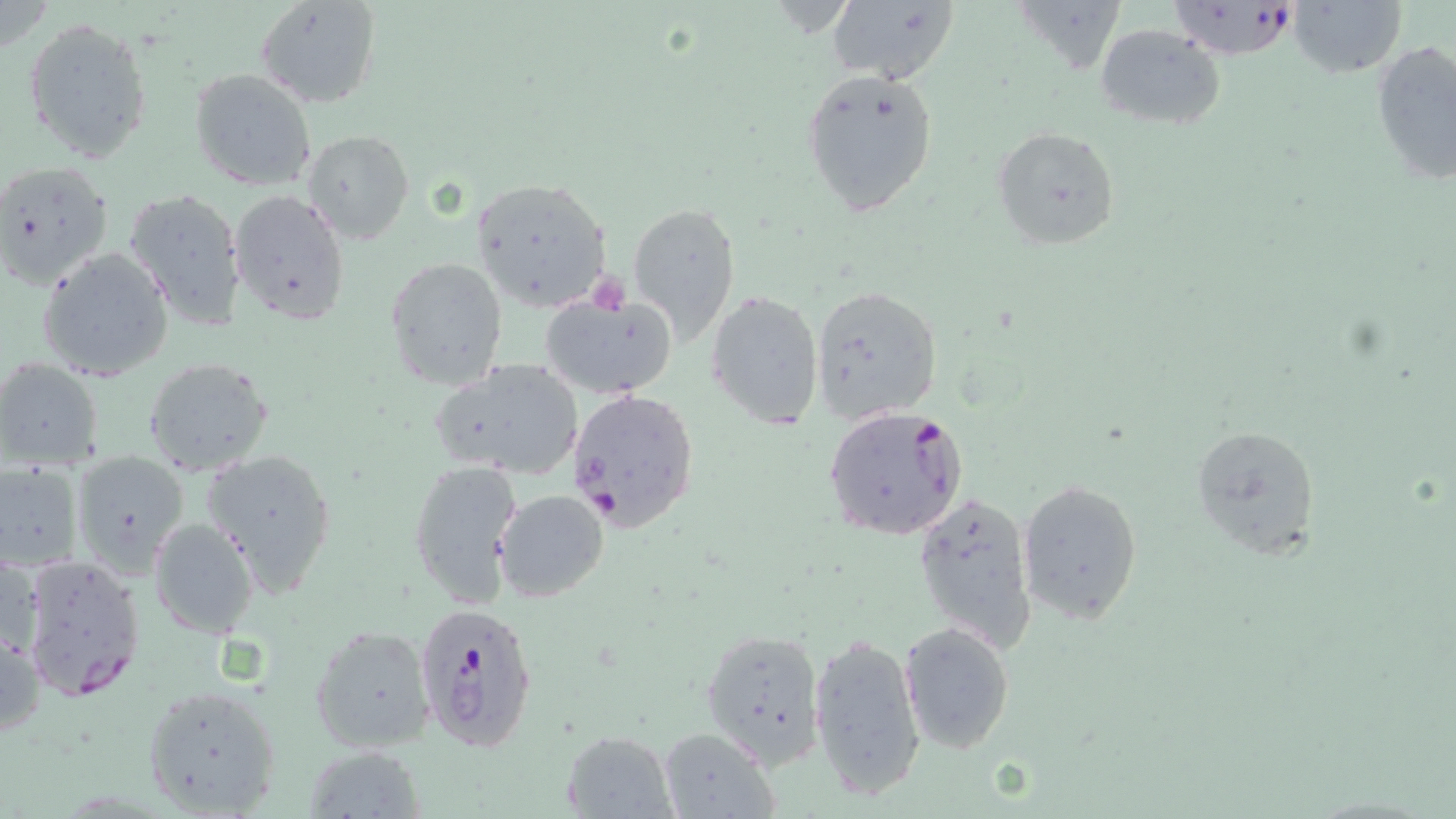

slide_level_diagnosis: Plasmodium falciparum
magnification: 1000x
field_of_view: one of a larger specimen
stain: May-Grünwald-Giemsa
plasmodium_falciparum_infected_red_blood_cell_locations: 'approximate bounding boxes as (x1,y1)-(x2,y2) corner pairs in pixels: (1166,2)-(1306,59), (566,386)-(700,532), (822,405)-(970,540), (20,554)-(146,701), (413,602)-(539,755)'
preparation: thin blood film
image_size: 1456×819 pixels
uninfected_red_blood_cell_locations: 'approximate bounding boxes as (x1,y1)-(x2,y2) corner pairs in pixels: (254,0)-(381,109), (1290,0)-(1406,80), (824,1)-(958,85), (24,16)-(152,165), (1095,23)-(1224,129), (1369,38)-(1456,186), (800,67)-(940,219), (188,69)-(317,193), (991,126)-(1121,252), (302,131)-(414,244), (1,159)-(113,288), (468,177)-(612,314), (124,188)-(246,330), (230,188)-(351,326), (628,200)-(739,344), (37,247)-(174,382), (385,255)-(508,389), (810,282)-(945,423), (707,290)-(823,432), (542,291)-(678,399), (142,356)-(274,477), (0,357)-(105,469), (430,358)-(584,480), (1189,423)-(1321,561), (202,446)-(338,595), (71,450)-(189,576), (407,459)-(521,608), (0,462)-(83,573), (1017,479)-(1143,624), (493,489)-(609,602), (912,489)-(1036,654), (149,517)-(259,637), (1,546)-(41,663), (902,621)-(1016,755), (309,624)-(436,752), (0,627)-(44,741), (701,627)-(824,766), (808,630)-(926,801), (139,680)-(284,818), (656,728)-(778,819), (562,729)-(679,817), (301,744)-(427,819)'
modality: optical microscopy